Name the parasite shown.
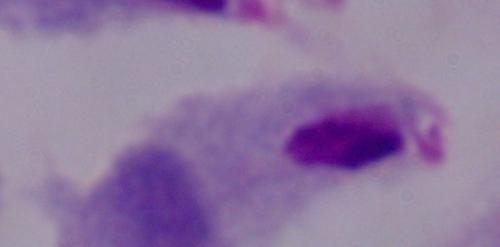

This is a trichomonad.

Photomicrograph. 1000x magnification.